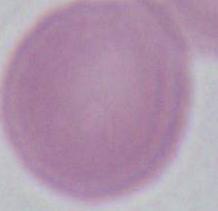

{
  "magnification": "1000x",
  "modality": "micrograph",
  "identification": "red blood cell"
}